Identify the blood parasite species.
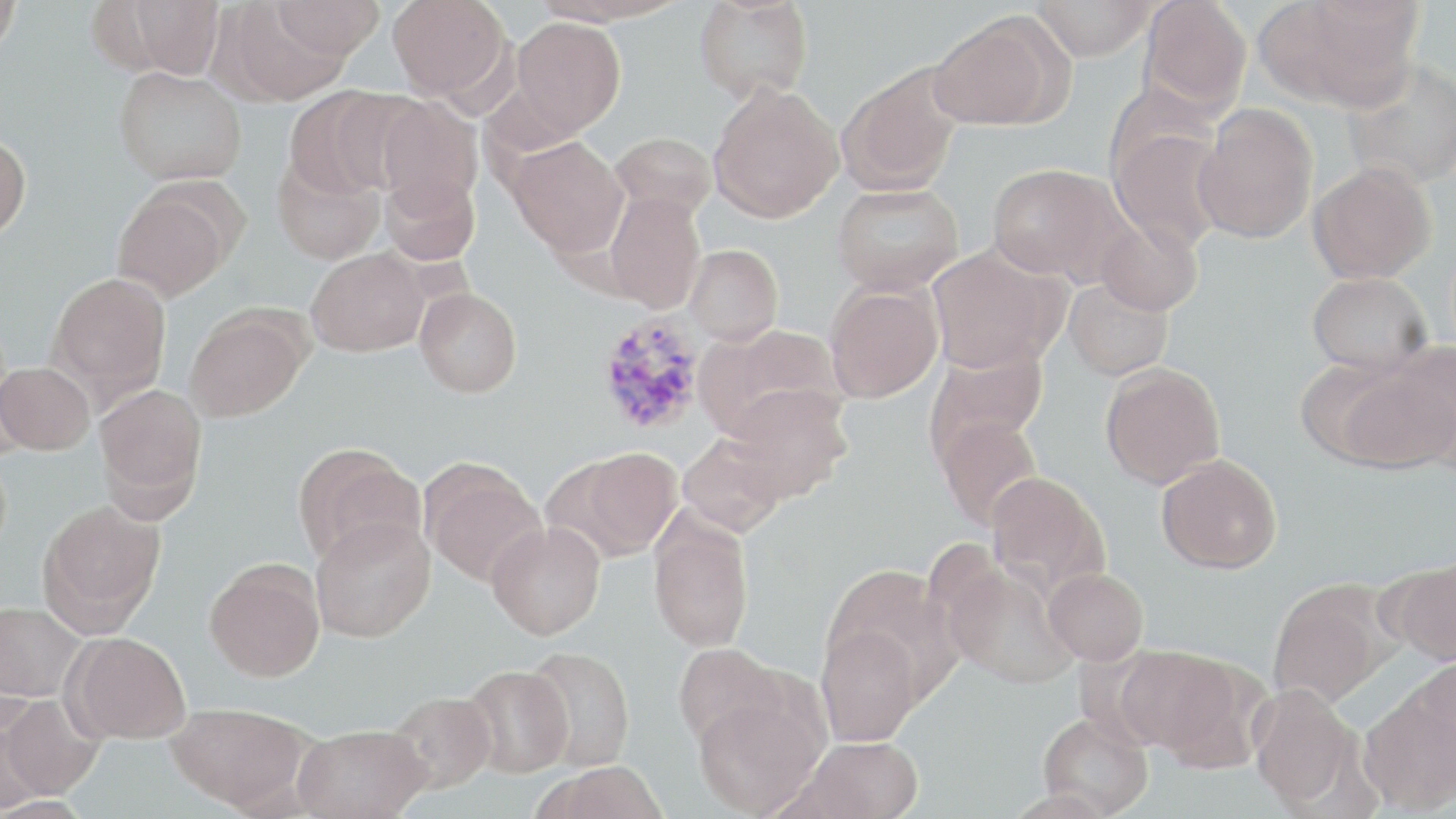
Plasmodium vivax.

{
  "uninfected_red_blood_cell_locations": "approximate bounding boxes as [x1, y1, x2, y2] in pixels: [0, 0, 21, 61], [272, 0, 385, 59], [387, 0, 509, 100], [694, 0, 814, 103], [1030, 0, 1155, 61], [1140, 0, 1252, 115], [1263, 0, 1423, 110], [122, 1, 225, 79], [220, 3, 352, 105], [927, 14, 1061, 131], [511, 17, 625, 136], [1341, 60, 1456, 191], [837, 63, 964, 196], [113, 66, 247, 185], [708, 83, 843, 223], [284, 86, 401, 199], [373, 96, 484, 211], [1192, 105, 1318, 244], [1108, 126, 1229, 251], [610, 131, 719, 221], [0, 132, 31, 243], [506, 136, 628, 257], [271, 153, 385, 265], [987, 163, 1126, 282], [1307, 163, 1436, 284], [380, 171, 480, 266], [831, 182, 965, 296], [110, 184, 235, 302], [605, 191, 705, 313], [1095, 216, 1203, 316], [685, 244, 783, 345], [306, 247, 430, 356], [927, 247, 1059, 373], [47, 272, 172, 399], [1306, 272, 1432, 377], [1063, 277, 1174, 381], [824, 283, 942, 403], [415, 287, 522, 398], [183, 305, 310, 422], [694, 324, 844, 441], [925, 342, 1049, 458], [1340, 348, 1456, 473], [1, 362, 95, 455], [1099, 362, 1226, 490], [93, 383, 208, 516], [720, 384, 852, 503], [935, 414, 1044, 531], [677, 432, 789, 536], [292, 442, 425, 568], [562, 447, 683, 560], [1156, 453, 1283, 574], [421, 458, 546, 587], [985, 471, 1111, 600], [39, 500, 166, 631], [648, 511, 754, 652], [311, 516, 435, 643], [486, 521, 606, 640], [204, 558, 326, 681], [1385, 560, 1456, 665], [943, 561, 1079, 690], [820, 564, 960, 698], [1044, 567, 1148, 664], [1267, 580, 1393, 709], [0, 599, 84, 703], [816, 622, 923, 746], [66, 632, 192, 743], [672, 642, 786, 749], [1115, 644, 1247, 759], [521, 646, 636, 771], [1414, 656, 1456, 769], [461, 664, 573, 778], [1249, 684, 1361, 809], [1358, 687, 1456, 815], [692, 689, 826, 817], [386, 690, 497, 793], [2, 693, 102, 799], [0, 701, 51, 812], [165, 702, 311, 811], [1036, 712, 1154, 817], [293, 724, 430, 819], [800, 736, 924, 819], [540, 762, 670, 819]",
  "plasmodium_vivax_infected_red_blood_cell_locations": "approximate bounding boxes as [x1, y1, x2, y2] in pixels: [595, 314, 708, 436]",
  "image_size": "1456×819 pixels",
  "stain": "May-Grünwald-Giemsa",
  "magnification": "1000x",
  "preparation": "thin blood film",
  "modality": "optical microscopy",
  "field_of_view": "one of a larger specimen"
}